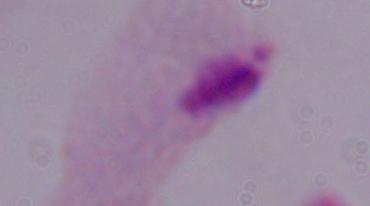
1000x magnification. A trichomonad is shown. Photomicrograph.